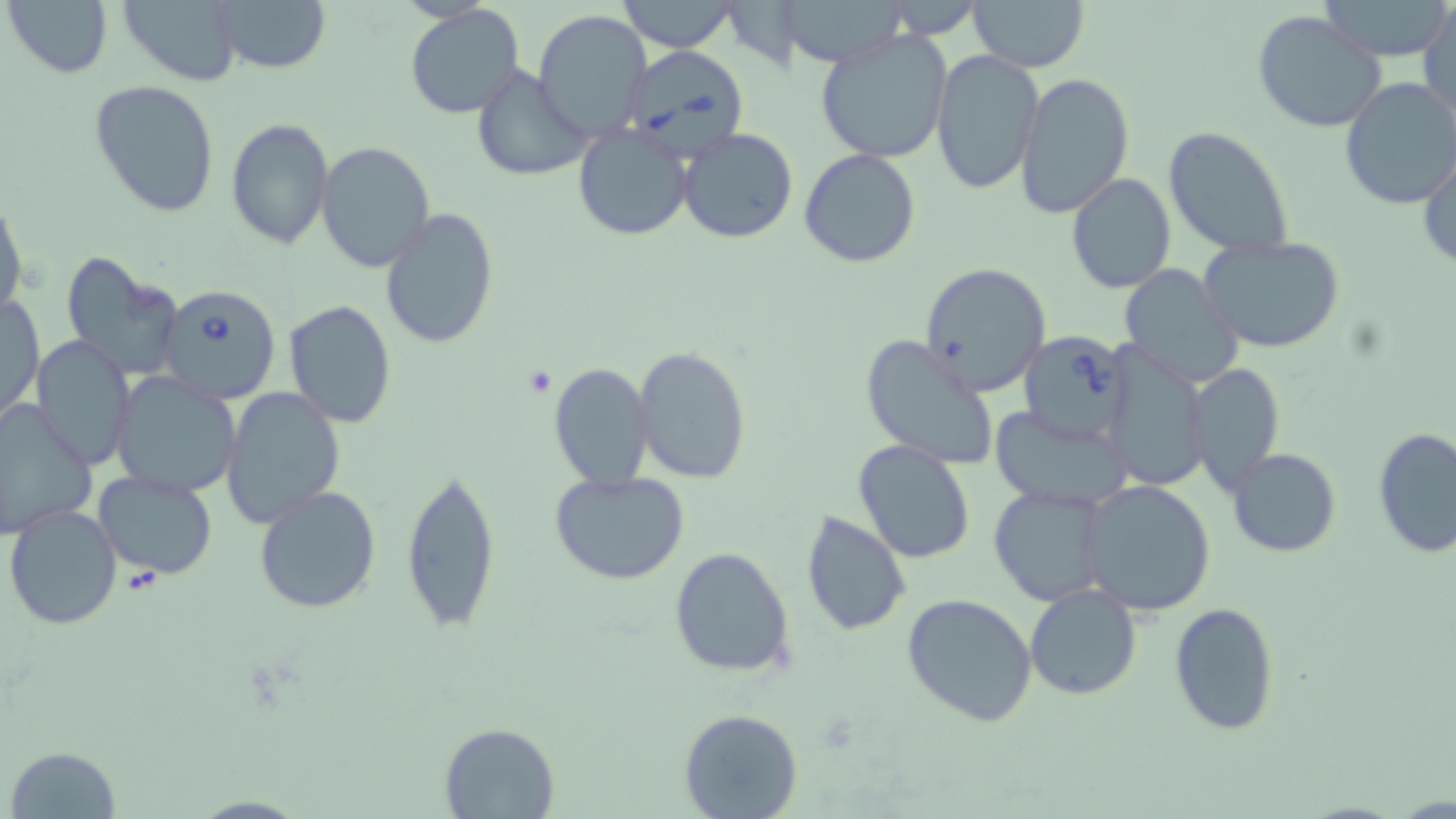

Approximate bounding boxes as named x1/y1/x2/y2 corners in pixels. Babesia divergens-infected red blood cell locations: (x1=621, y1=46, x2=749, y2=161), (x1=155, y1=282, x2=283, y2=403), (x1=1014, y1=330, x2=1134, y2=445). Uninfected red blood cell locations: (x1=3, y1=0, x2=114, y2=79), (x1=119, y1=0, x2=243, y2=85), (x1=210, y1=0, x2=330, y2=72), (x1=613, y1=0, x2=742, y2=53), (x1=777, y1=0, x2=911, y2=69), (x1=970, y1=0, x2=1089, y2=73), (x1=1320, y1=0, x2=1455, y2=61), (x1=1420, y1=3, x2=1455, y2=127), (x1=406, y1=4, x2=525, y2=118), (x1=533, y1=9, x2=652, y2=139), (x1=1251, y1=9, x2=1387, y2=134), (x1=814, y1=29, x2=953, y2=162), (x1=931, y1=49, x2=1044, y2=196), (x1=468, y1=64, x2=591, y2=182), (x1=1014, y1=72, x2=1136, y2=219), (x1=1338, y1=76, x2=1456, y2=212), (x1=89, y1=79, x2=220, y2=216), (x1=224, y1=116, x2=334, y2=250), (x1=574, y1=122, x2=693, y2=240), (x1=1163, y1=126, x2=1293, y2=259), (x1=676, y1=128, x2=798, y2=243), (x1=316, y1=141, x2=435, y2=272), (x1=1418, y1=143, x2=1456, y2=271), (x1=799, y1=149, x2=921, y2=268), (x1=1066, y1=173, x2=1177, y2=294), (x1=0, y1=195, x2=27, y2=320), (x1=379, y1=207, x2=499, y2=350), (x1=1198, y1=235, x2=1347, y2=355), (x1=58, y1=250, x2=182, y2=378), (x1=918, y1=262, x2=1052, y2=399), (x1=1118, y1=265, x2=1245, y2=389), (x1=2, y1=293, x2=44, y2=423), (x1=284, y1=300, x2=396, y2=427), (x1=860, y1=334, x2=1000, y2=470), (x1=30, y1=336, x2=135, y2=470), (x1=633, y1=345, x2=751, y2=484), (x1=1100, y1=348, x2=1211, y2=491), (x1=547, y1=361, x2=655, y2=491), (x1=1185, y1=362, x2=1286, y2=496), (x1=110, y1=372, x2=242, y2=498), (x1=221, y1=386, x2=345, y2=529), (x1=0, y1=399, x2=97, y2=540), (x1=989, y1=406, x2=1136, y2=513), (x1=1373, y1=428, x2=1456, y2=557), (x1=851, y1=440, x2=976, y2=566), (x1=1227, y1=448, x2=1342, y2=557), (x1=401, y1=462, x2=502, y2=634), (x1=93, y1=470, x2=219, y2=581), (x1=549, y1=470, x2=691, y2=585), (x1=1079, y1=479, x2=1220, y2=616), (x1=990, y1=483, x2=1108, y2=605), (x1=253, y1=485, x2=382, y2=614), (x1=4, y1=504, x2=123, y2=630), (x1=800, y1=509, x2=913, y2=637), (x1=668, y1=548, x2=795, y2=679), (x1=1024, y1=584, x2=1143, y2=700), (x1=902, y1=592, x2=1038, y2=728), (x1=1169, y1=602, x2=1279, y2=736), (x1=680, y1=709, x2=802, y2=819), (x1=439, y1=721, x2=560, y2=818), (x1=7, y1=746, x2=121, y2=817). Slide-level diagnosis: Babesia divergens. Single field of view. Thin blood smear. May-Grünwald-Giemsa stain. Captured at 1000x magnification. Image is 1456×819 pixels. Light microscopy.